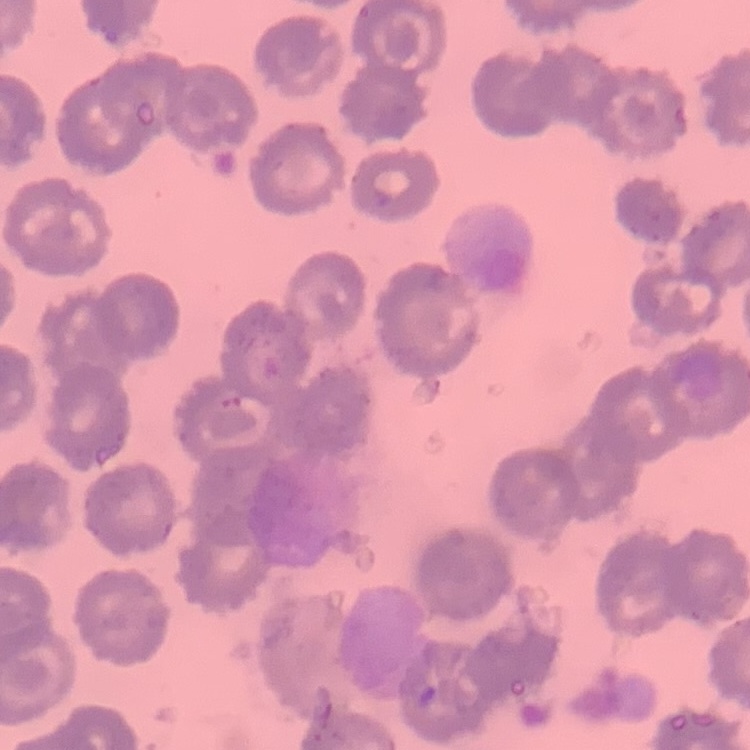
{
  "erythrocyte_morphology": "no rouleaux formation",
  "preparation": "thin peripheral smear",
  "stain": "Field's or Giemsa",
  "image_type": "square crop of a larger photomicrograph"
}